Report the malaria status of this cell.
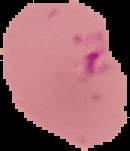

Parasitized.

From a thin blood smear. The area outside the segmented cell region is set to black. Image is 130×151 pixels.